Classify this cell by malaria status.
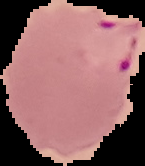
It is parasitized.

Segmented cell region on a black background. Image is 145×166 pixels. From a thin blood smear.